Identify the preparation type.
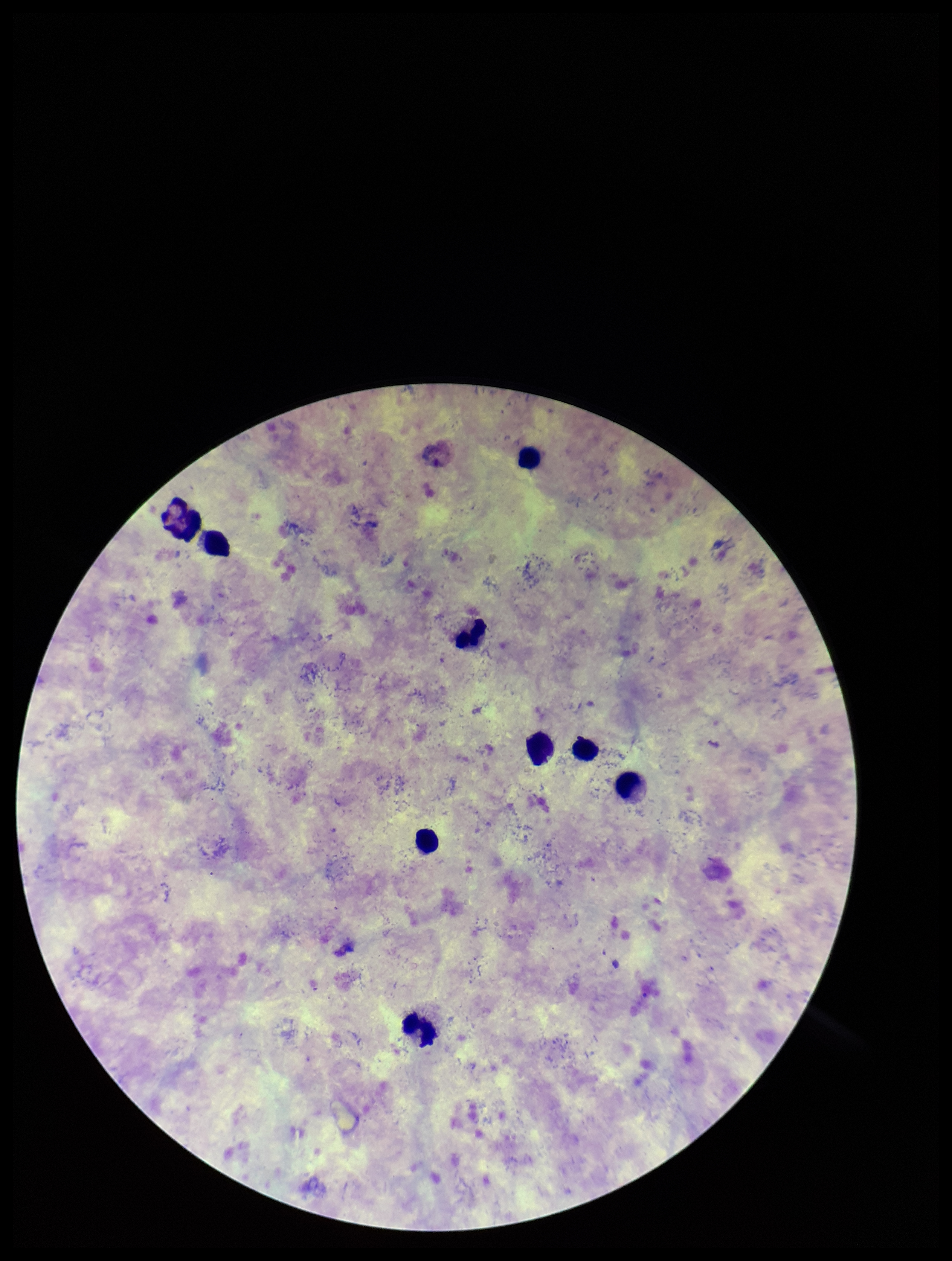
A thick smear.

Summary:
  - Parasite count: 0
  - Image size: 952×1261 pixels
  - Plasmodium parasites: none detected
  - Capture: smartphone photograph through the microscope eyepiece
  - Patient malaria status: infected
  - Species reported for this patient: Plasmodium vivax
  - Leukocyte count: 9
  - Stain: Giemsa
  - Field of view: single